Classify this cell by malaria status.
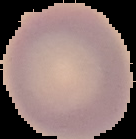
It is uninfected.

Cell region segmented out of the field of view; the surrounding area is masked to black. From a thin blood smear. Image is 136×139 pixels.